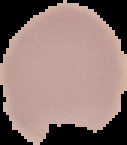

Summary:
  - Image type: cell region segmented out of the field of view; surrounding area masked to black
  - Malaria status: uninfected
  - Image size: 127×145 pixels
  - Preparation: thin blood smear